Name the parasite shown.
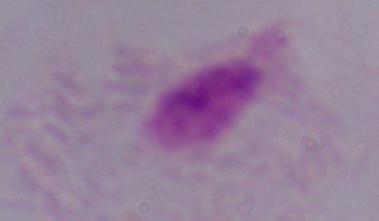

A trichomonad.

magnification = 1000x
modality = micrograph